Locate every blood parasite and identify its species.
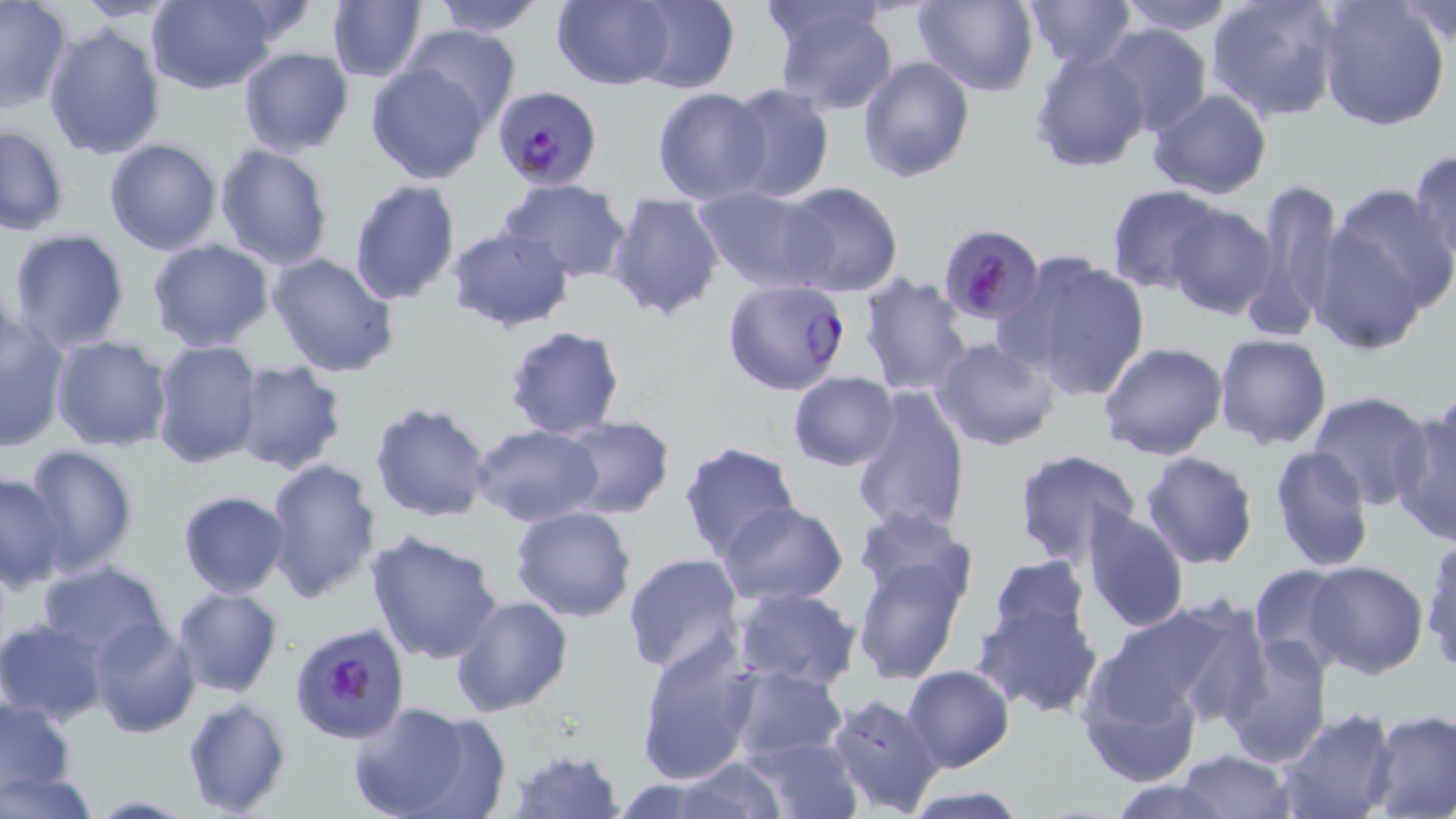
Approximate bounding boxes as (x1,y1)-(x2,y2) corner pairs in pixels.
Plasmodium falciparum-infected red blood cells: (492,84)-(602,191), (937,224)-(1044,325), (723,278)-(850,394), (289,622)-(413,747).
No Plasmodium ovale, Plasmodium malariae, Plasmodium vivax, Babesia divergens, or Trypanosoma brucei observed.

Summary:
  - Uninfected red blood cell locations: (75,0)-(178,22), (146,0)-(284,95), (427,0)-(551,37), (553,0)-(675,89), (627,0)-(740,93), (912,0)-(1039,96), (1021,0)-(1139,68), (1114,0)-(1240,35), (1206,0)-(1344,123), (1316,1)-(1450,131), (1395,1)-(1456,51), (326,2)-(428,81), (768,2)-(901,116), (0,4)-(71,113), (43,22)-(165,162), (1096,22)-(1212,138), (402,24)-(520,130), (1029,45)-(1150,172), (238,46)-(354,156), (857,56)-(975,183), (366,63)-(490,183), (721,84)-(835,202), (652,87)-(773,204), (1148,89)-(1273,199), (0,124)-(70,235), (104,139)-(223,254), (214,144)-(334,270), (1408,148)-(1455,264), (499,178)-(631,279), (1250,178)-(1343,333), (348,179)-(461,306), (781,182)-(903,299), (1328,182)-(1456,312), (694,184)-(833,294), (1107,185)-(1224,295), (606,192)-(725,321), (1165,204)-(1279,321), (446,226)-(574,333), (1311,226)-(1427,354), (7,228)-(131,352), (147,238)-(273,351), (267,251)-(400,378), (1004,253)-(1152,401), (860,272)-(976,394), (0,313)-(71,452), (504,325)-(626,441), (1214,334)-(1332,451), (50,335)-(173,452), (933,337)-(1060,452), (150,340)-(263,469), (1098,342)-(1228,462), (229,362)-(347,475), (788,370)-(900,470), (851,384)-(971,537), (1307,393)-(1435,511), (369,400)-(494,523), (1391,402)-(1456,545), (558,416)-(674,519), (469,423)-(603,527), (678,442)-(801,565), (21,445)-(139,577), (1269,445)-(1375,571), (1012,447)-(1142,567), (1141,451)-(1258,569), (264,457)-(381,602), (0,472)-(72,591), (177,491)-(289,597), (718,501)-(849,606), (511,506)-(638,622), (1080,506)-(1190,633), (851,508)-(976,616), (365,530)-(506,665), (1421,535)-(1456,674), (850,547)-(973,686), (623,553)-(746,676), (987,554)-(1090,642), (36,560)-(171,666), (1250,563)-(1352,672), (1303,563)-(1431,679), (172,587)-(282,697), (729,588)-(861,693), (449,595)-(573,717), (1088,600)-(1257,737), (972,601)-(1103,717), (0,619)-(108,726), (87,619)-(201,738), (635,636)-(759,784), (1219,637)-(1332,767), (1076,639)-(1215,788), (725,664)-(850,764), (903,664)-(1013,772), (825,693)-(947,816), (0,696)-(78,798), (182,698)-(291,816), (349,701)-(498,819), (1368,709)-(1456,817), (1275,710)-(1399,819), (741,736)-(864,818), (508,745)-(627,819), (1175,750)-(1296,819), (675,758)-(789,817), (1,768)-(97,819), (1103,778)-(1240,818), (901,786)-(1031,818), (81,795)-(199,818)
  - Slide-level diagnosis: Plasmodium falciparum
  - Preparation: thin blood smear
  - Modality: light microscopy
  - Image size: 1456×819 pixels
  - Magnification: 1000x
  - Field of view: one of a larger specimen
  - Stain: May-Grünwald-Giemsa